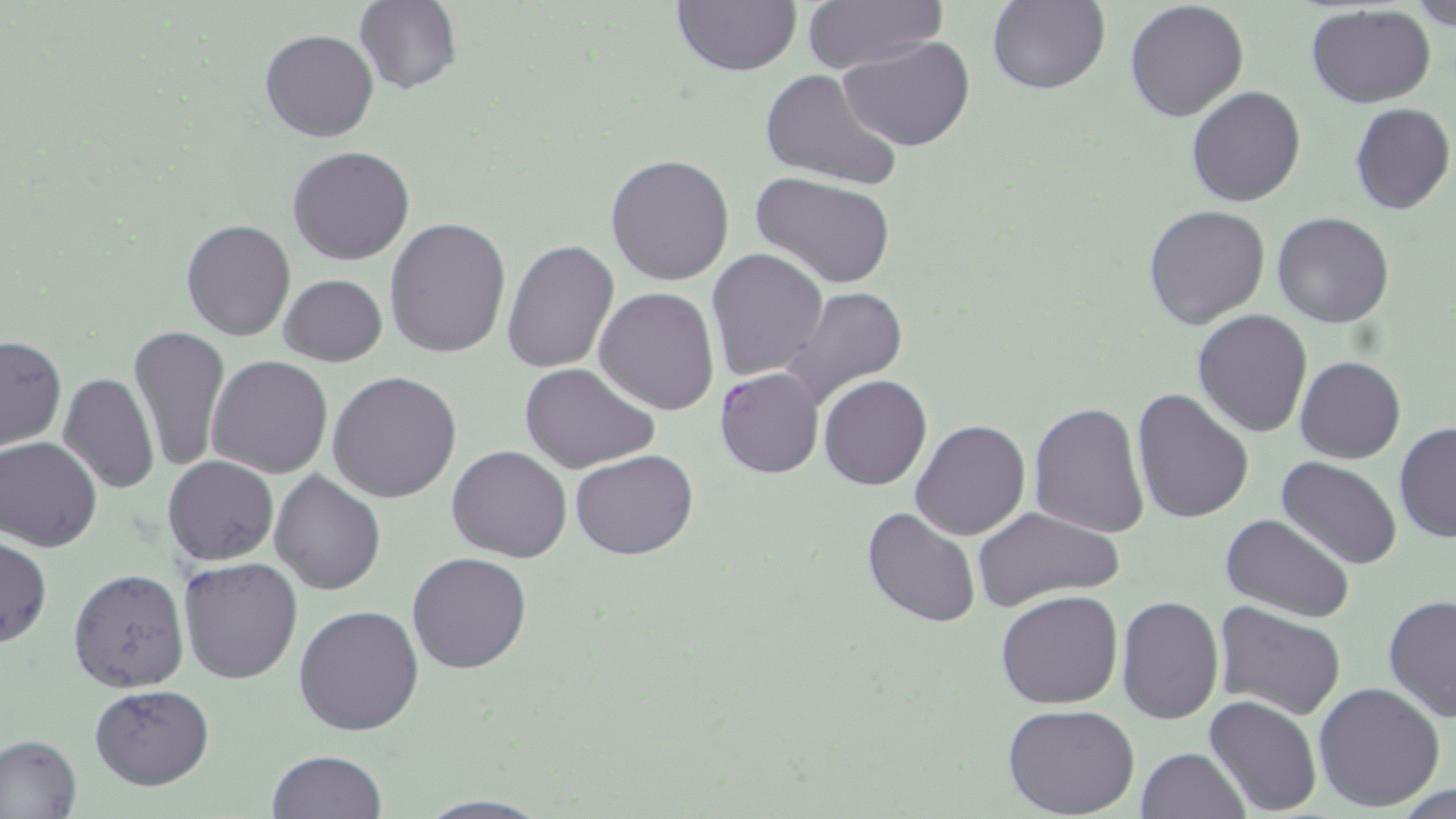
{
  "slide_level_diagnosis": "Plasmodium falciparum",
  "stain": "May-Grünwald-Giemsa",
  "magnification": "1000x",
  "field_of_view": "single",
  "image_size": "1456×819 pixels",
  "modality": "optical microscopy",
  "uninfected_red_blood_cell_locations": "approximate bounding boxes as (x1,y1)-(x2,y2) corner pairs in pixels: (670,0)-(803,77), (800,0)-(948,74), (1411,0)-(1456,29), (355,1)-(462,95), (986,1)-(1111,95), (1124,1)-(1249,122), (1304,5)-(1436,108), (261,29)-(379,143), (839,38)-(977,152), (759,69)-(903,192), (1186,86)-(1306,207), (1349,102)-(1455,215), (287,146)-(415,265), (605,153)-(735,286), (753,173)-(896,289), (1144,206)-(1270,329), (1272,211)-(1396,327), (181,218)-(296,341), (385,218)-(512,358), (501,239)-(619,375), (707,249)-(829,380), (279,273)-(388,367), (781,286)-(909,412), (594,287)-(720,415), (1192,309)-(1313,438), (128,325)-(232,473), (0,335)-(67,451), (207,355)-(331,477), (1296,355)-(1405,463), (203,363)-(450,488), (520,363)-(661,473), (58,371)-(158,493), (327,371)-(462,504), (819,375)-(932,490), (1131,388)-(1254,523), (1029,401)-(1149,541), (911,418)-(1031,540), (1394,420)-(1456,544), (1,437)-(102,551), (447,445)-(573,562), (571,450)-(697,560), (163,455)-(279,566), (1277,456)-(1402,570), (269,470)-(385,594), (863,506)-(981,628), (972,506)-(1125,615), (1221,513)-(1353,622), (0,536)-(51,649), (407,553)-(533,673), (178,556)-(305,685), (69,568)-(190,691), (996,590)-(1123,709), (1117,594)-(1224,723), (1383,594)-(1456,723), (1214,600)-(1347,719), (293,603)-(425,737), (1312,682)-(1446,812), (89,683)-(215,789), (1204,695)-(1323,817), (1004,705)-(1140,819), (0,732)-(82,819), (1137,747)-(1248,819), (266,750)-(387,819), (413,794)-(553,818)",
  "preparation": "thin blood smear",
  "plasmodium_falciparum_infected_red_blood_cell_locations": "approximate bounding boxes as (x1,y1)-(x2,y2) corner pairs in pixels: (714,366)-(824,479)"
}